Classify the preparation.
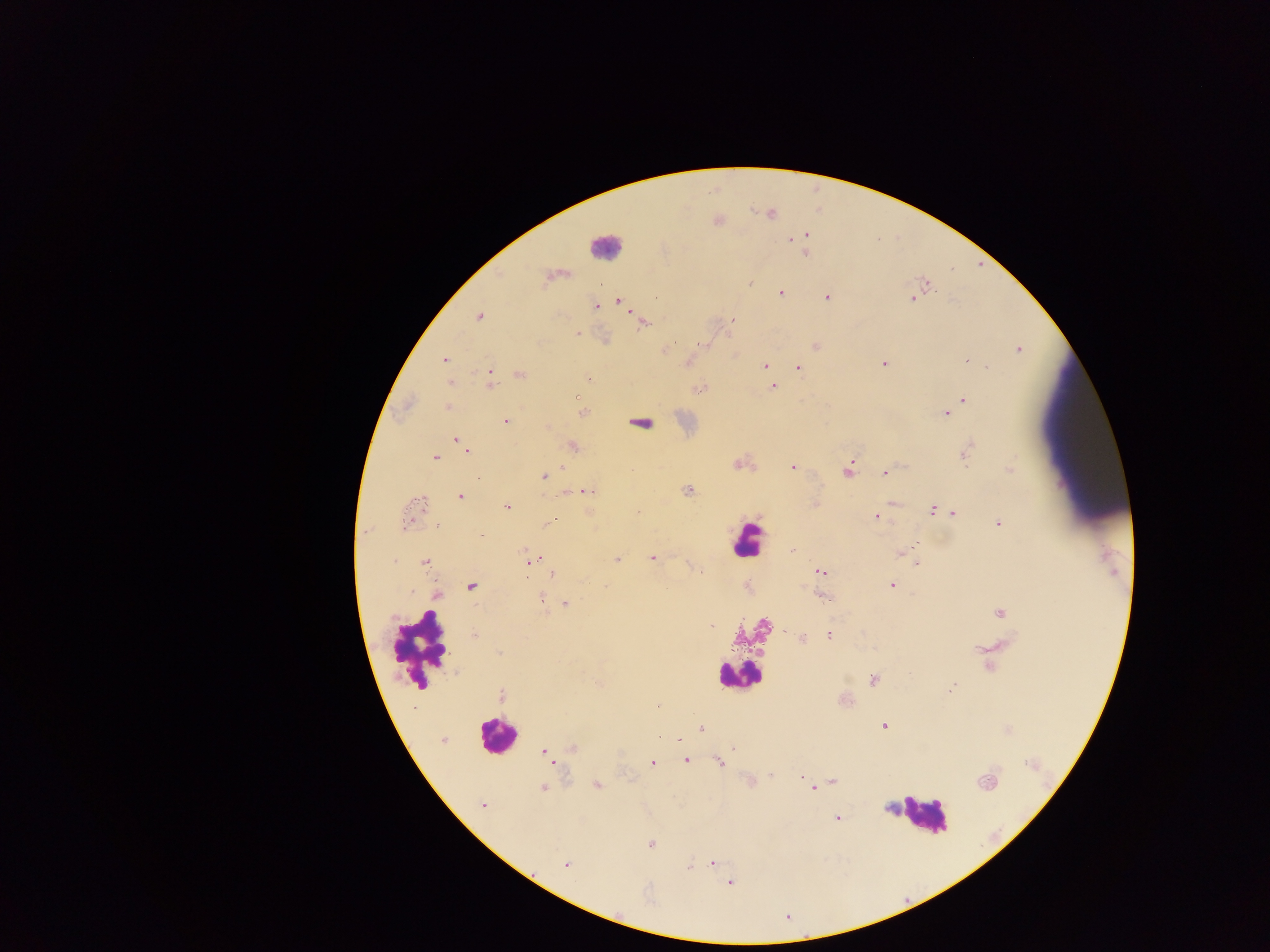
Thick blood film.

{
  "malaria_parasite_locations": "approximate centers as {x, y} in pixels: {804, 236}, {789, 239}, {805, 253}, {546, 280}, {750, 284}, {926, 284}, {780, 293}, {827, 297}, {619, 300}, {913, 300}, {596, 306}, {479, 317}, {733, 320}, {644, 323}, {576, 333}, {674, 343}, {815, 347}, {1018, 349}, {445, 359}, {966, 361}, {884, 363}, {764, 366}, {798, 367}, {988, 367}, {520, 374}, {589, 379}, {489, 381}, {450, 382}, {773, 387}, {699, 389}, {575, 398}, {964, 400}, {448, 406}, {582, 413}, {946, 414}, {505, 421}, {640, 423}, {457, 440}, {573, 446}, {466, 450}, {967, 452}, {436, 458}, {737, 465}, {792, 467}, {1010, 469}, {847, 471}, {885, 472}, {543, 476}, {478, 478}, {688, 490}, {584, 491}, {460, 497}, {418, 503}, {894, 503}, {507, 507}, {932, 509}, {953, 513}, {875, 517}, {549, 522}, {405, 523}, {998, 524}, {438, 525}, {365, 532}, {916, 545}, {524, 550}, {794, 550}, {900, 553}, {652, 557}, {618, 559}, {395, 561}, {528, 561}, {425, 562}, {917, 564}, {821, 571}, {700, 572}, {553, 574}, {891, 585}, {471, 586}, {606, 586}, {437, 595}, {821, 597}, {541, 599}, {566, 604}, {1000, 612}, {711, 626}, {786, 632}, {475, 635}, {829, 636}, {801, 638}, {499, 652}, {873, 680}, {599, 684}, {951, 689}, {502, 696}, {884, 726}, {701, 728}, {659, 737}, {443, 740}, {734, 747}, {573, 748}, {544, 752}, {686, 760}, {553, 761}, {652, 763}, {719, 763}, {770, 775}, {801, 777}, {832, 781}, {985, 783}, {597, 785}, {542, 788}, {813, 789}, {483, 806}, {838, 818}, {651, 843}, {712, 863}, {565, 865}, {690, 867}, {730, 882}",
  "field_of_view": "single",
  "leukocyte_locations": "approximate centers as {x, y} in pixels: {605, 246}, {748, 540}, {418, 650}, {739, 677}, {496, 735}, {923, 814}",
  "capture": "mobile-phone photograph through a microscope",
  "country": "Ghana",
  "image_size": "1270×952 pixels"
}